Locate every Plasmodium parasite.
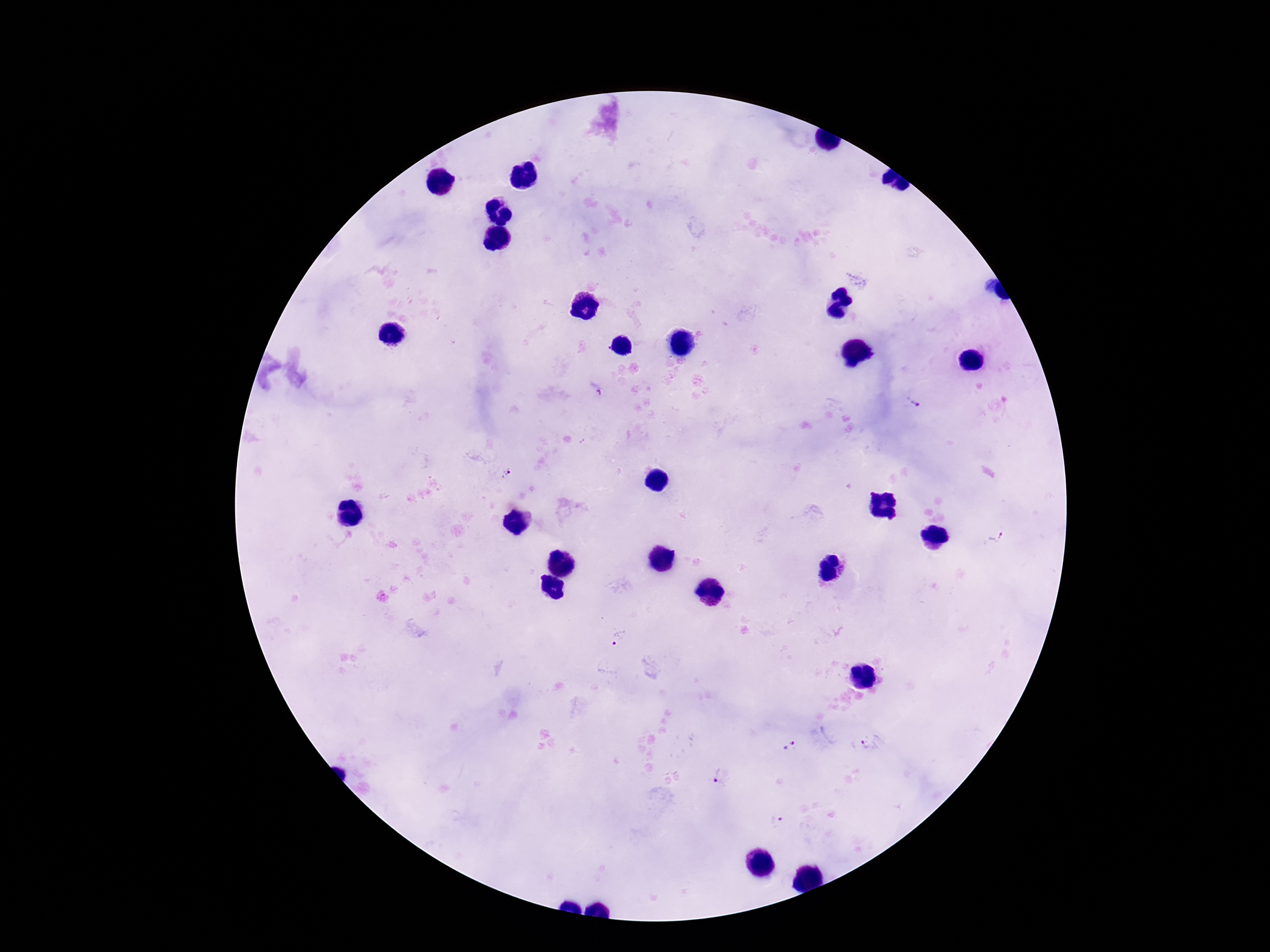

Approximate object centers, in pixels from the top-left corner.
Plasmodium parasites: (x=597, y=388), (x=913, y=402), (x=508, y=473), (x=993, y=538), (x=619, y=638), (x=870, y=743), (x=791, y=746), (x=717, y=775), (x=775, y=820).

preparation = thick peripheral-blood smear
stain = Giemsa
capture = smartphone camera through the microscope eyepiece
patient malaria status = positive
field of view = one from this slide
magnification = 100x
image size = 1270×952 pixels